Report the malaria status of this cell.
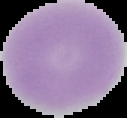

Uninfected.

image_type: segmented cell region with the area outside set to black
preparation: thin blood film
image_size: 127×118 pixels